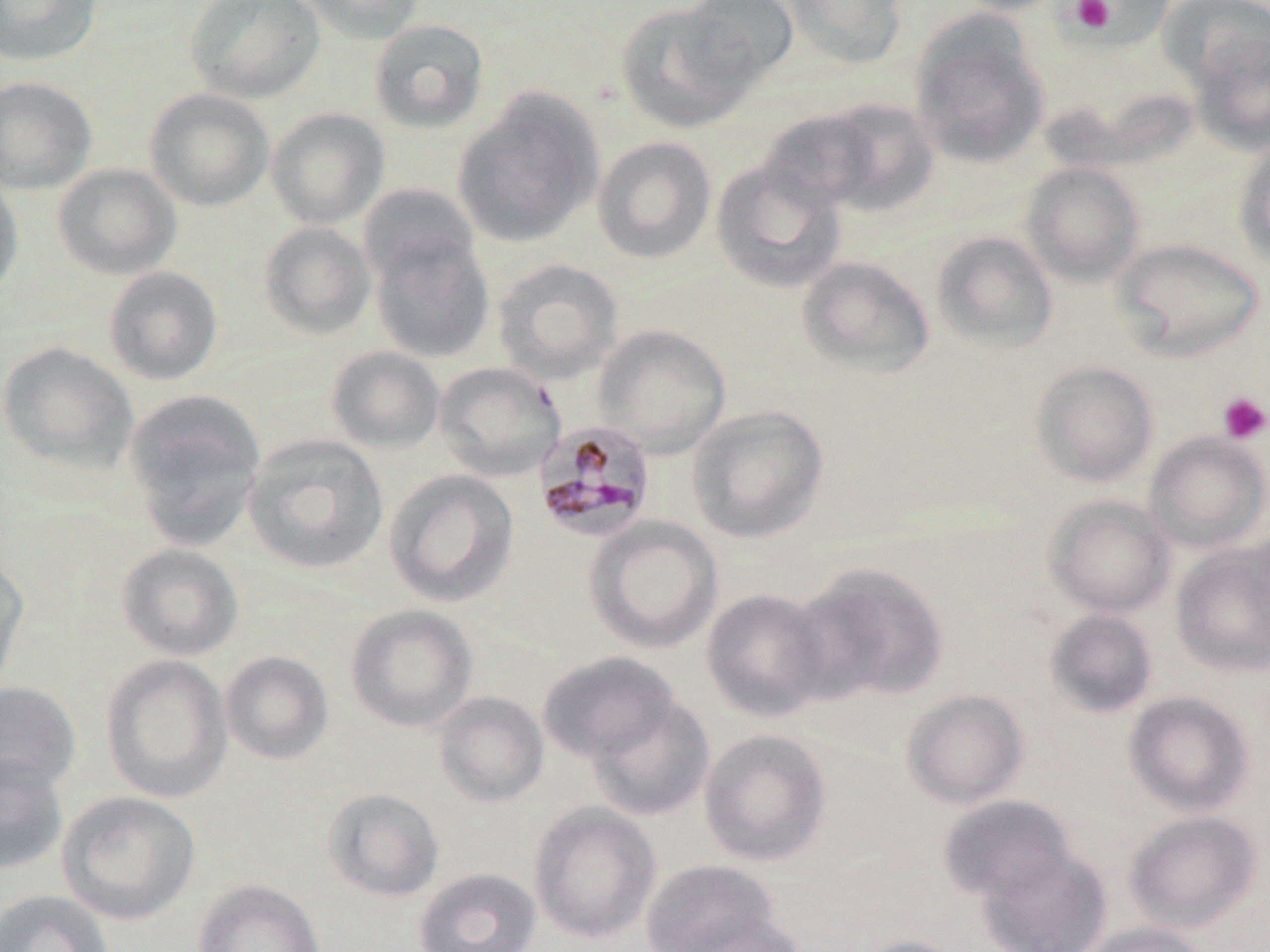

slide-level diagnosis = Plasmodium malariae
field of view = single
stain = May-Grünwald-Giemsa
preparation = thin blood film
Plasmodium malariae-infected red blood cell locations = approximate bounding boxes as named x1/y1/x2/y2 corners in pixels: (x1=533, y1=419, x2=656, y2=541)
platelet locations = approximate bounding boxes as named x1/y1/x2/y2 corners in pixels: (x1=1064, y1=0, x2=1154, y2=42), (x1=1071, y1=0, x2=1114, y2=33), (x1=1217, y1=392, x2=1269, y2=444)
image size = 1270×952 pixels
modality = light microscopy
magnification = 1000x
uninfected red blood cell locations = approximate bounding boxes as named x1/y1/x2/y2 corners in pixels: (x1=0, y1=0, x2=103, y2=66), (x1=186, y1=0, x2=326, y2=104), (x1=298, y1=0, x2=427, y2=45), (x1=680, y1=0, x2=799, y2=85), (x1=779, y1=0, x2=907, y2=70), (x1=950, y1=0, x2=1069, y2=15), (x1=1069, y1=0, x2=1175, y2=51), (x1=1156, y1=1, x2=1270, y2=93), (x1=614, y1=2, x2=759, y2=133), (x1=909, y1=14, x2=1050, y2=169), (x1=369, y1=18, x2=489, y2=133), (x1=1188, y1=28, x2=1269, y2=153), (x1=0, y1=76, x2=98, y2=195), (x1=144, y1=87, x2=275, y2=212), (x1=453, y1=89, x2=604, y2=249), (x1=816, y1=99, x2=940, y2=216), (x1=265, y1=108, x2=390, y2=229), (x1=758, y1=108, x2=882, y2=212), (x1=592, y1=136, x2=717, y2=264), (x1=1234, y1=138, x2=1270, y2=267), (x1=711, y1=160, x2=846, y2=293), (x1=1021, y1=161, x2=1145, y2=286), (x1=52, y1=163, x2=182, y2=280), (x1=0, y1=171, x2=24, y2=302), (x1=359, y1=183, x2=479, y2=288), (x1=259, y1=222, x2=376, y2=338), (x1=368, y1=227, x2=494, y2=364), (x1=931, y1=230, x2=1058, y2=353), (x1=1112, y1=238, x2=1264, y2=361), (x1=796, y1=256, x2=935, y2=378), (x1=492, y1=258, x2=624, y2=385), (x1=103, y1=266, x2=224, y2=386), (x1=593, y1=325, x2=731, y2=456), (x1=0, y1=341, x2=139, y2=475), (x1=325, y1=345, x2=445, y2=453), (x1=1030, y1=360, x2=1159, y2=488), (x1=433, y1=361, x2=567, y2=482), (x1=122, y1=388, x2=267, y2=547), (x1=686, y1=404, x2=830, y2=543), (x1=1144, y1=431, x2=1270, y2=552), (x1=242, y1=433, x2=389, y2=575), (x1=384, y1=469, x2=519, y2=607), (x1=1044, y1=494, x2=1175, y2=617), (x1=584, y1=516, x2=723, y2=654), (x1=1170, y1=542, x2=1270, y2=676), (x1=115, y1=543, x2=244, y2=661), (x1=0, y1=556, x2=30, y2=697), (x1=792, y1=561, x2=951, y2=705), (x1=701, y1=587, x2=833, y2=722), (x1=345, y1=604, x2=477, y2=731), (x1=1045, y1=608, x2=1159, y2=718), (x1=220, y1=651, x2=333, y2=765), (x1=537, y1=652, x2=681, y2=765), (x1=100, y1=654, x2=232, y2=803), (x1=0, y1=682, x2=81, y2=797), (x1=901, y1=688, x2=1029, y2=809), (x1=1123, y1=690, x2=1254, y2=817), (x1=432, y1=691, x2=549, y2=807), (x1=586, y1=694, x2=715, y2=822), (x1=699, y1=728, x2=832, y2=867), (x1=0, y1=753, x2=69, y2=876), (x1=322, y1=788, x2=444, y2=902), (x1=57, y1=791, x2=200, y2=925), (x1=938, y1=794, x2=1076, y2=904), (x1=528, y1=801, x2=662, y2=945), (x1=1124, y1=810, x2=1263, y2=934), (x1=977, y1=847, x2=1112, y2=952), (x1=642, y1=859, x2=780, y2=952), (x1=413, y1=868, x2=541, y2=952), (x1=192, y1=879, x2=324, y2=952), (x1=0, y1=889, x2=113, y2=952), (x1=676, y1=912, x2=807, y2=952), (x1=1079, y1=921, x2=1210, y2=952), (x1=853, y1=935, x2=967, y2=952)